Classify this cell by malaria status.
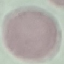
Uninfected.

Summary:
  - Capture: smartphone through the microscope eyepiece
  - Stain: Giemsa
  - Preparation: thin blood smear
  - Image type: cell patch, automatically extracted from a larger field of view and resized to 64 × 64 pixels